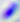
Photomicrograph. Captured at 400x magnification. Toxoplasma gondii is shown.